State which parasite is depicted.
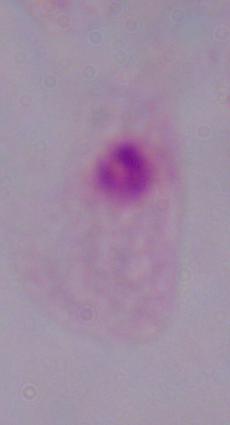

A trichomonad.

{
  "magnification": "1000x",
  "modality": "micrograph"
}